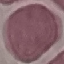
Summary:
  - Malaria status: uninfected
  - Capture: smartphone camera at the microscope eyepiece
  - Stain: Giemsa
  - Image type: cell patch, automatically extracted from a larger field of view and resized to 64 × 64 pixels
  - Preparation: thin blood smear